Point out leukocytes.
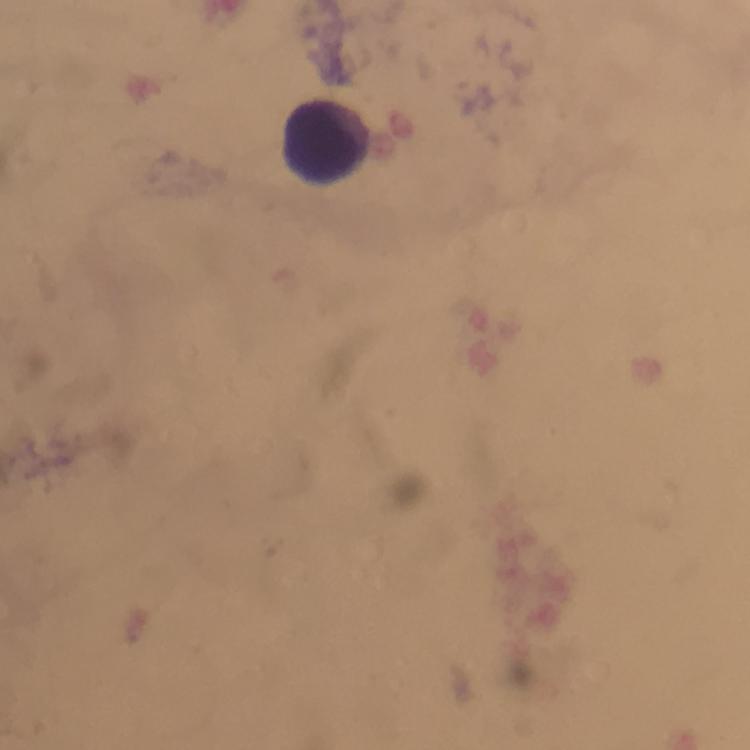

Approximate centers as [x, y] in pixels.
Leukocytes: [325, 142].

Giemsa stain. Thick blood smear. Plasmodium parasites: none seen. Image is 750×750 pixels. Cropped region of a single field of view. Immersion oil was used. From a malaria diagnostic workup. Smartphone photograph taken through a microscope. At 100x magnification.